Describe the morphology of the red blood cells.
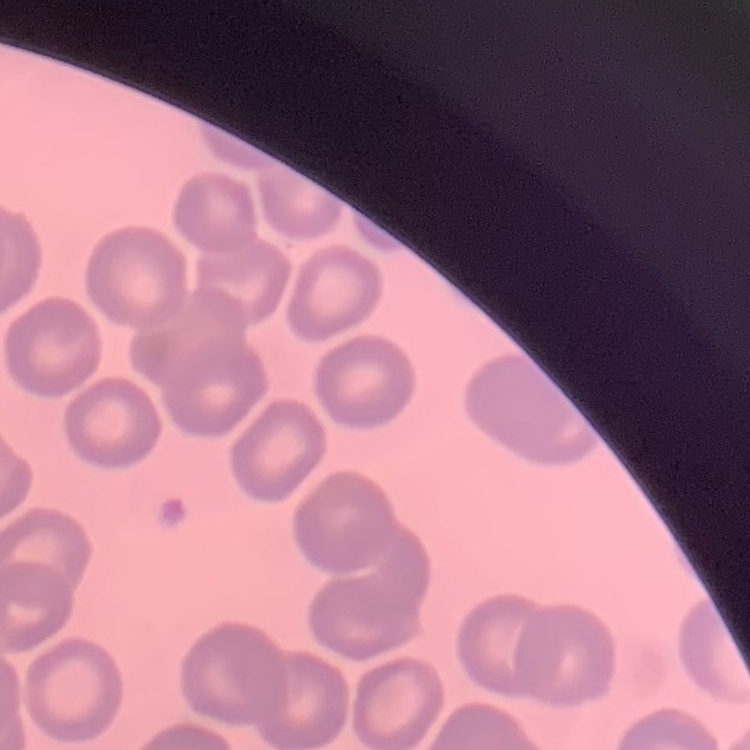
No rouleaux formation.

Summary:
  - Stain: Field's or Giemsa
  - Preparation: thin peripheral smear
  - Image type: one tile cut from a larger photomicrograph